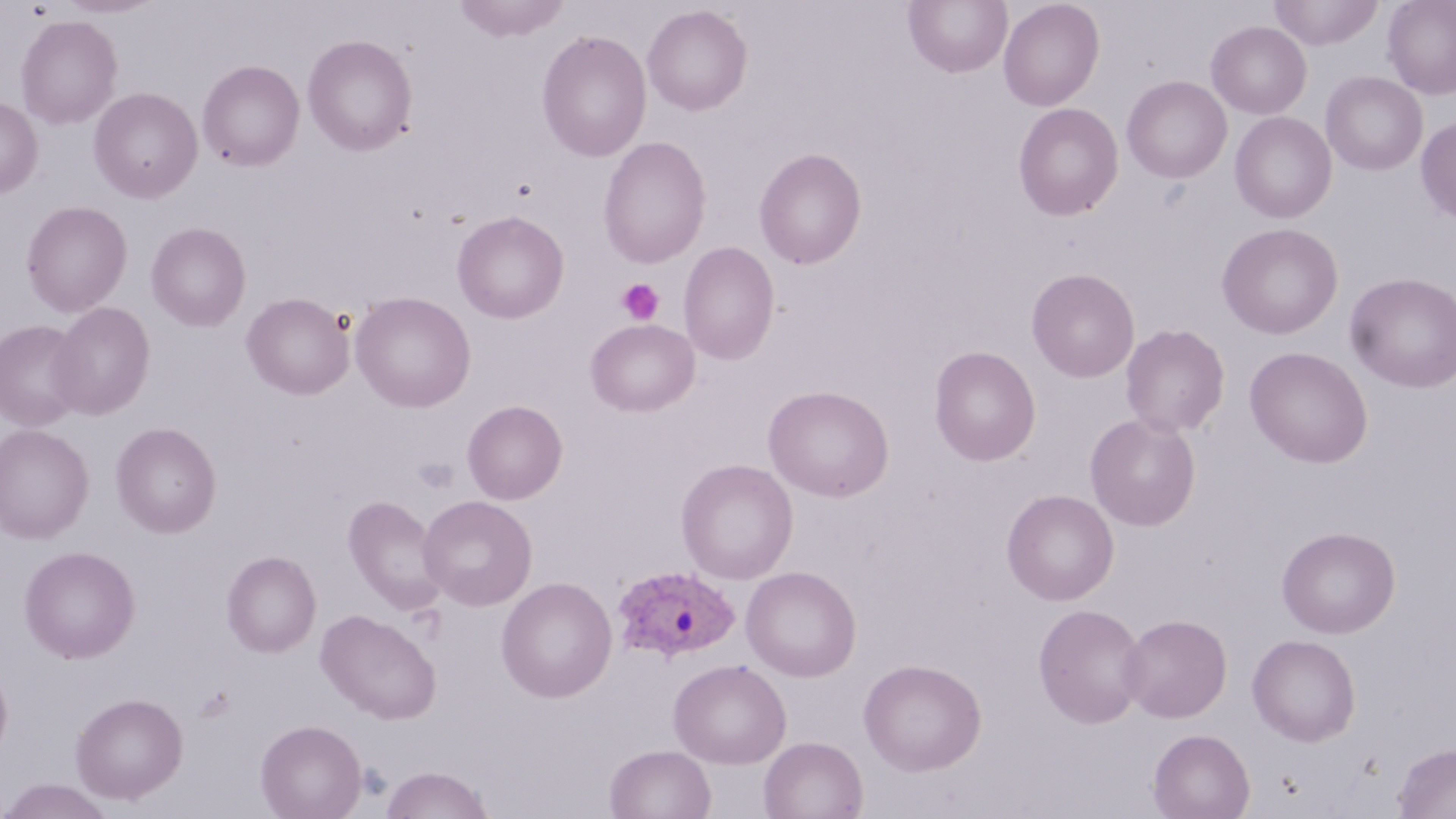
Approximate bounding boxes as named x1/y1/x2/y2 corners in pixels. Uninfected red blood cell locations: (x1=56, y1=0, x2=161, y2=18), (x1=452, y1=0, x2=570, y2=42), (x1=998, y1=0, x2=1105, y2=111), (x1=1268, y1=0, x2=1384, y2=49), (x1=1382, y1=0, x2=1456, y2=99), (x1=904, y1=1, x2=1012, y2=78), (x1=642, y1=5, x2=752, y2=115), (x1=15, y1=15, x2=123, y2=129), (x1=1206, y1=20, x2=1312, y2=118), (x1=536, y1=29, x2=652, y2=162), (x1=302, y1=34, x2=417, y2=156), (x1=197, y1=59, x2=305, y2=171), (x1=1321, y1=72, x2=1428, y2=176), (x1=1122, y1=75, x2=1232, y2=183), (x1=88, y1=87, x2=202, y2=203), (x1=0, y1=97, x2=42, y2=198), (x1=1013, y1=102, x2=1123, y2=220), (x1=1230, y1=112, x2=1337, y2=223), (x1=1416, y1=116, x2=1456, y2=223), (x1=597, y1=136, x2=711, y2=269), (x1=754, y1=147, x2=867, y2=269), (x1=20, y1=200, x2=132, y2=317), (x1=36, y1=201, x2=142, y2=419), (x1=452, y1=209, x2=569, y2=324), (x1=146, y1=222, x2=251, y2=331), (x1=1217, y1=222, x2=1343, y2=339), (x1=678, y1=242, x2=780, y2=365), (x1=1026, y1=267, x2=1140, y2=382), (x1=1345, y1=272, x2=1456, y2=393), (x1=350, y1=291, x2=476, y2=413), (x1=241, y1=292, x2=354, y2=400), (x1=48, y1=302, x2=155, y2=420), (x1=585, y1=318, x2=699, y2=416), (x1=0, y1=319, x2=86, y2=432), (x1=1120, y1=324, x2=1230, y2=437), (x1=929, y1=345, x2=1041, y2=466), (x1=1244, y1=346, x2=1373, y2=468), (x1=764, y1=384, x2=894, y2=502), (x1=462, y1=400, x2=567, y2=504), (x1=1085, y1=413, x2=1200, y2=531), (x1=110, y1=422, x2=221, y2=538), (x1=0, y1=424, x2=94, y2=543), (x1=676, y1=458, x2=799, y2=584), (x1=1002, y1=489, x2=1119, y2=605), (x1=418, y1=495, x2=537, y2=610), (x1=343, y1=496, x2=448, y2=614), (x1=1277, y1=526, x2=1401, y2=638), (x1=19, y1=545, x2=140, y2=663), (x1=221, y1=550, x2=321, y2=657), (x1=741, y1=565, x2=861, y2=682), (x1=496, y1=576, x2=617, y2=702), (x1=1033, y1=603, x2=1148, y2=728), (x1=316, y1=609, x2=441, y2=724), (x1=1119, y1=614, x2=1232, y2=722), (x1=1247, y1=634, x2=1361, y2=746), (x1=668, y1=658, x2=791, y2=768), (x1=859, y1=658, x2=986, y2=775), (x1=0, y1=661, x2=13, y2=764), (x1=71, y1=692, x2=188, y2=804), (x1=255, y1=719, x2=366, y2=819), (x1=1149, y1=728, x2=1254, y2=819), (x1=759, y1=736, x2=868, y2=819), (x1=1394, y1=743, x2=1455, y2=819), (x1=604, y1=744, x2=715, y2=819), (x1=380, y1=766, x2=494, y2=818), (x1=0, y1=778, x2=116, y2=819). Plasmodium ovale-infected red blood cell locations: (x1=611, y1=564, x2=740, y2=663). Platelet locations: (x1=617, y1=278, x2=664, y2=325), (x1=412, y1=457, x2=458, y2=493). Slide-level diagnosis: Plasmodium ovale. Single field of view. Thin blood smear. Image is 1456×819 pixels. May-Grünwald-Giemsa-stained preparation. Optical microscopy. 1000x magnification.